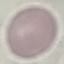
Malaria status: uninfected. Thin blood film. Photographed with a smartphone camera at the microscope eyepiece. Giemsa stain. Cell patch, automatically extracted from a larger field of view and resized to 64 × 64 pixels.